Identify the blood parasite species.
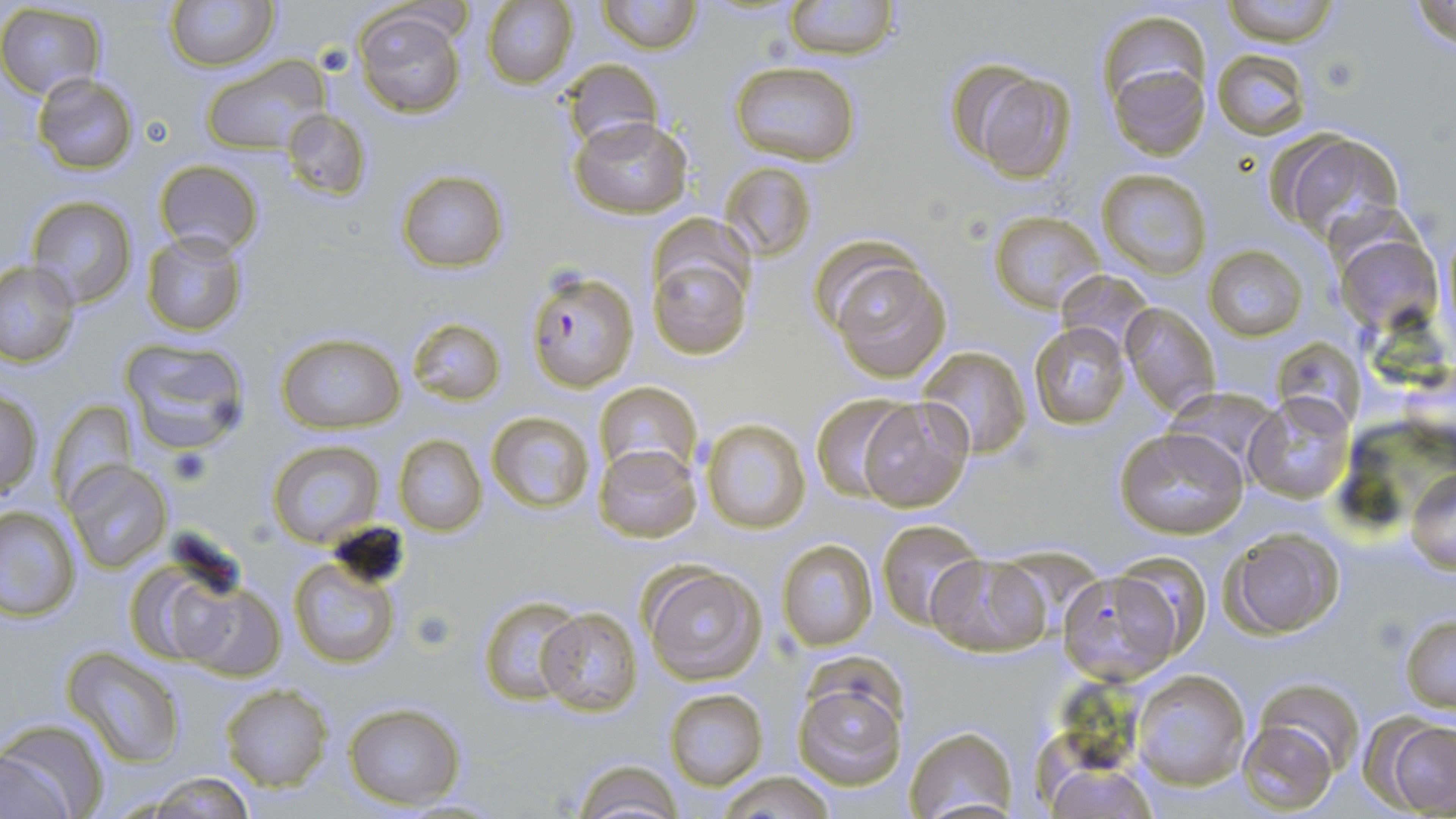
Plasmodium falciparum.

stain = May-Grünwald-Giemsa
magnification = 1000x
Plasmodium falciparum-infected red blood cell locations = approximate bounding boxes as named x1/y1/x2/y2 corners in pixels: (x1=524, y1=267, x2=640, y2=392)
platelet locations = approximate bounding boxes as named x1/y1/x2/y2 corners in pixels: (x1=1317, y1=54, x2=1362, y2=95), (x1=167, y1=445, x2=213, y2=488), (x1=409, y1=606, x2=458, y2=653)
field of view = one of a larger specimen
uninfected red blood cell locations = approximate bounding boxes as named x1/y1/x2/y2 corners in pixels: (x1=166, y1=0, x2=279, y2=70), (x1=598, y1=0, x2=700, y2=53), (x1=782, y1=0, x2=901, y2=60), (x1=1219, y1=0, x2=1344, y2=45), (x1=1408, y1=0, x2=1456, y2=54), (x1=480, y1=1, x2=577, y2=88), (x1=0, y1=3, x2=106, y2=99), (x1=353, y1=8, x2=467, y2=117), (x1=1098, y1=12, x2=1212, y2=120), (x1=1212, y1=48, x2=1309, y2=138), (x1=201, y1=55, x2=329, y2=156), (x1=560, y1=57, x2=663, y2=151), (x1=728, y1=62, x2=861, y2=167), (x1=1110, y1=63, x2=1209, y2=161), (x1=959, y1=64, x2=1075, y2=182), (x1=31, y1=73, x2=140, y2=173), (x1=279, y1=107, x2=373, y2=201), (x1=569, y1=118, x2=691, y2=220), (x1=1271, y1=129, x2=1407, y2=247), (x1=153, y1=158, x2=266, y2=255), (x1=720, y1=161, x2=815, y2=262), (x1=396, y1=170, x2=509, y2=273), (x1=1098, y1=170, x2=1211, y2=278), (x1=24, y1=195, x2=137, y2=308), (x1=988, y1=210, x2=1108, y2=312), (x1=141, y1=231, x2=249, y2=336), (x1=1334, y1=233, x2=1443, y2=335), (x1=647, y1=244, x2=753, y2=360), (x1=1204, y1=246, x2=1309, y2=341), (x1=825, y1=256, x2=952, y2=382), (x1=0, y1=262, x2=79, y2=366), (x1=1056, y1=273, x2=1152, y2=355), (x1=1121, y1=302, x2=1220, y2=416), (x1=407, y1=317, x2=506, y2=405), (x1=1029, y1=322, x2=1131, y2=429), (x1=277, y1=331, x2=405, y2=435), (x1=119, y1=337, x2=253, y2=457), (x1=1273, y1=338, x2=1367, y2=431), (x1=919, y1=346, x2=1032, y2=457), (x1=593, y1=381, x2=702, y2=479), (x1=1162, y1=385, x2=1284, y2=481), (x1=0, y1=389, x2=44, y2=497), (x1=810, y1=393, x2=915, y2=501), (x1=1243, y1=393, x2=1356, y2=504), (x1=856, y1=396, x2=974, y2=513), (x1=47, y1=399, x2=137, y2=506), (x1=487, y1=411, x2=594, y2=512), (x1=699, y1=418, x2=812, y2=535), (x1=1113, y1=426, x2=1248, y2=538), (x1=394, y1=435, x2=487, y2=536), (x1=267, y1=439, x2=383, y2=549), (x1=593, y1=446, x2=700, y2=543), (x1=64, y1=461, x2=172, y2=573), (x1=1408, y1=473, x2=1456, y2=571), (x1=0, y1=505, x2=80, y2=620), (x1=876, y1=519, x2=984, y2=628), (x1=1220, y1=526, x2=1345, y2=638), (x1=776, y1=539, x2=878, y2=651), (x1=290, y1=550, x2=403, y2=670), (x1=125, y1=552, x2=255, y2=667), (x1=925, y1=554, x2=1051, y2=658), (x1=639, y1=563, x2=766, y2=684), (x1=1058, y1=569, x2=1185, y2=685), (x1=174, y1=582, x2=284, y2=679), (x1=478, y1=596, x2=582, y2=706), (x1=535, y1=607, x2=642, y2=714), (x1=1400, y1=615, x2=1456, y2=711), (x1=65, y1=649, x2=185, y2=767), (x1=1131, y1=668, x2=1251, y2=790), (x1=792, y1=674, x2=910, y2=791), (x1=1250, y1=677, x2=1367, y2=781), (x1=220, y1=685, x2=332, y2=790), (x1=664, y1=689, x2=768, y2=788), (x1=343, y1=702, x2=465, y2=810), (x1=1369, y1=714, x2=1456, y2=817), (x1=1238, y1=719, x2=1338, y2=813), (x1=0, y1=721, x2=106, y2=819), (x1=903, y1=726, x2=1018, y2=817), (x1=569, y1=759, x2=688, y2=819), (x1=1042, y1=762, x2=1161, y2=818), (x1=719, y1=771, x2=833, y2=819), (x1=141, y1=773, x2=259, y2=816)
preparation = thin blood film
modality = light microscopy
image size = 1456×819 pixels